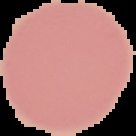

Summary:
  - Image type: cell region segmented out of the field of view; surrounding area masked to black
  - Result: no Plasmodium parasites detected
  - Image size: 136×136 pixels
  - Preparation: thin blood film